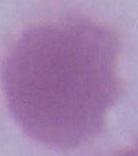

Summary:
  - Modality: micrograph
  - Identification: erythrocyte
  - Magnification: 1000x